Comment on the morphology of the erythrocytes.
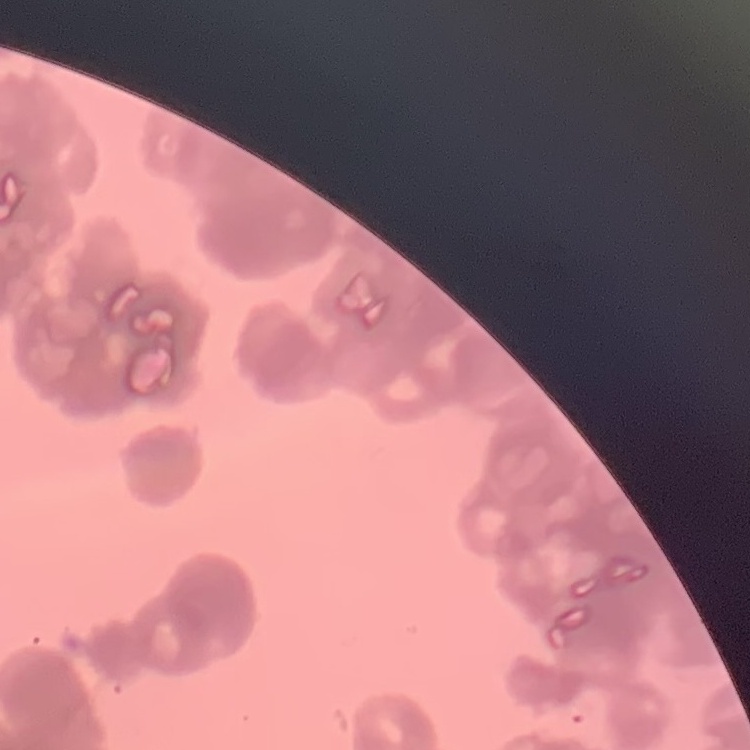

Rouleaux formation.

Summary:
  - Preparation: thin blood smear
  - Image type: square crop of a larger photomicrograph
  - Stain: Field's or Giemsa